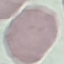
result = no malaria parasites detected
preparation = thin blood smear
capture = smartphone camera at the microscope eyepiece
stain = Giemsa
image type = automatically extracted cell patch, resized to 64 × 64 pixels